Identify the parasite.
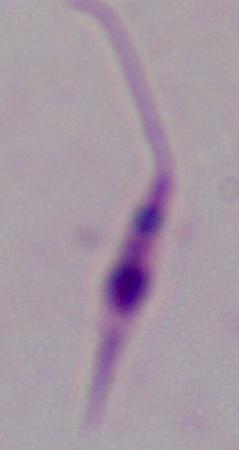

Leishmania.

Summary:
  - Magnification: 1000x
  - Modality: micrograph